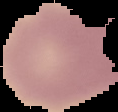

Summary:
  - Image type: segmented cell region with the area outside set to black
  - Image size: 118×112 pixels
  - Preparation: thin blood film
  - Malaria status: uninfected